Name the parasite shown.
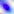
This is Toxoplasma gondii.

{
  "modality": "micrograph",
  "magnification": "400x"
}